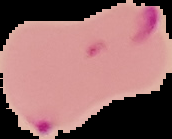

From a thin blood film. Malaria status: parasitized. The area outside the segmented cell region is set to black. Image is 172×139 pixels.